Name the cell type shown.
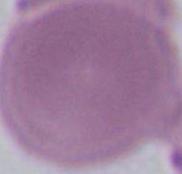

An erythrocyte.

Summary:
  - Magnification: 1000x
  - Modality: micrograph